State which cell type is depicted.
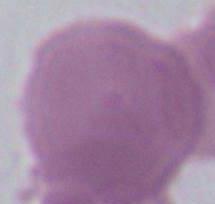
This is an erythrocyte.

1000x magnification. Photomicrograph.